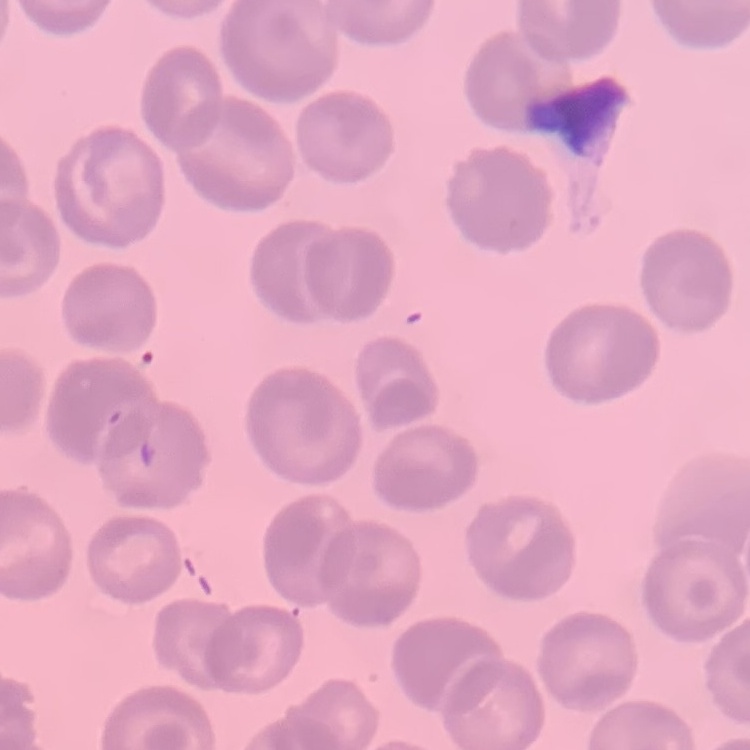
The erythrocytes exhibit no rouleaux formation. Thin blood film. Field's or Giemsa stain. One tile cut from a larger photomicrograph.